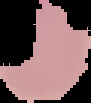

image_size: 91×103 pixels
image_type: segmented cell region on a black background
preparation: thin blood film
malaria_status: parasitized